Comment on the morphology of the erythrocytes.
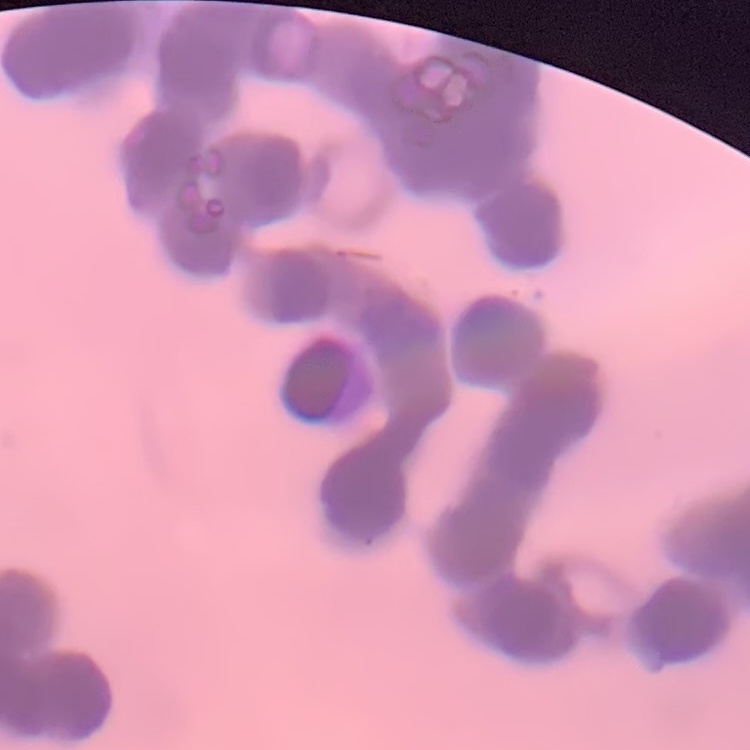

Rouleaux formation.

Square crop of a larger photomicrograph. Stained with either Field's or Giemsa. Thin blood smear.